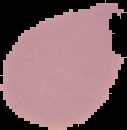

Summary:
  - Image size: 127×130 pixels
  - Result: no malaria parasites seen
  - Image type: cell region segmented out of the field of view; surrounding area masked to black
  - Preparation: thin blood film